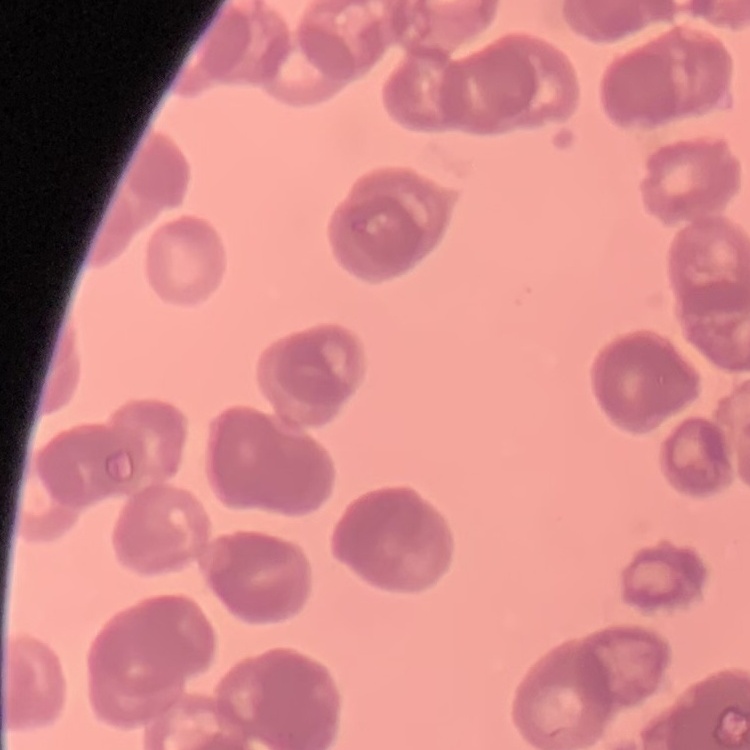

Summary:
  - Erythrocyte morphology: rouleaux formation
  - Stain: Field's or Giemsa
  - Preparation: thin blood film
  - Image type: one tile cut from a larger photomicrograph